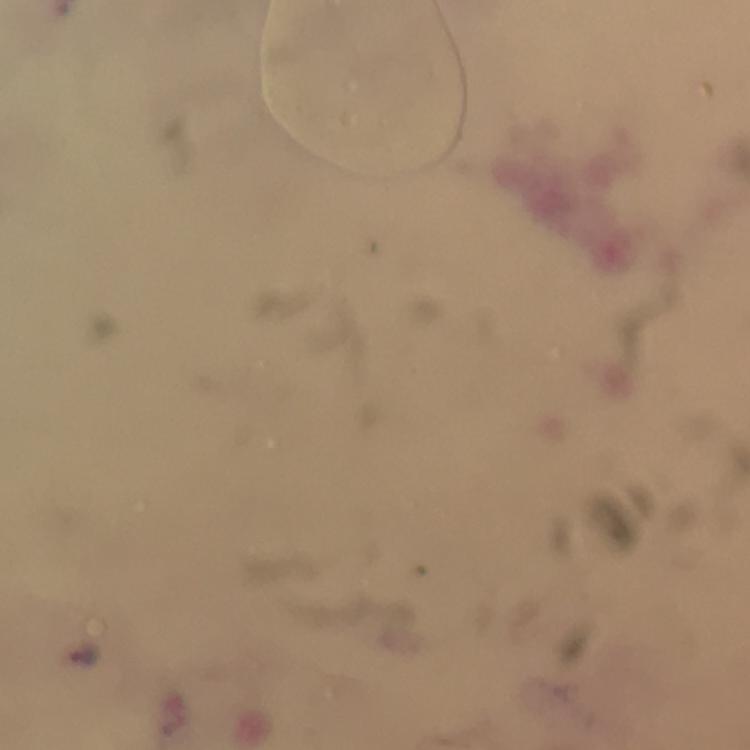
preparation = thick blood smear
image size = 750×750 pixels
stain = Giemsa
magnification = 100x
context = from a diagnostic examination for malaria
cropped from = one field of view
capture = smartphone photograph through a microscope
malaria parasite locations = approximate centers as {x, y} in pixels: {84, 654}
immersion oil = applied